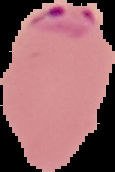 Result: malaria parasites detected. Cell region segmented out of the field of view; the surrounding area is masked to black. From a thin blood smear. Image is 115×172 pixels.